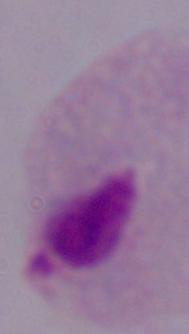
A trichomonad is shown. Micrograph. 1000x magnification.